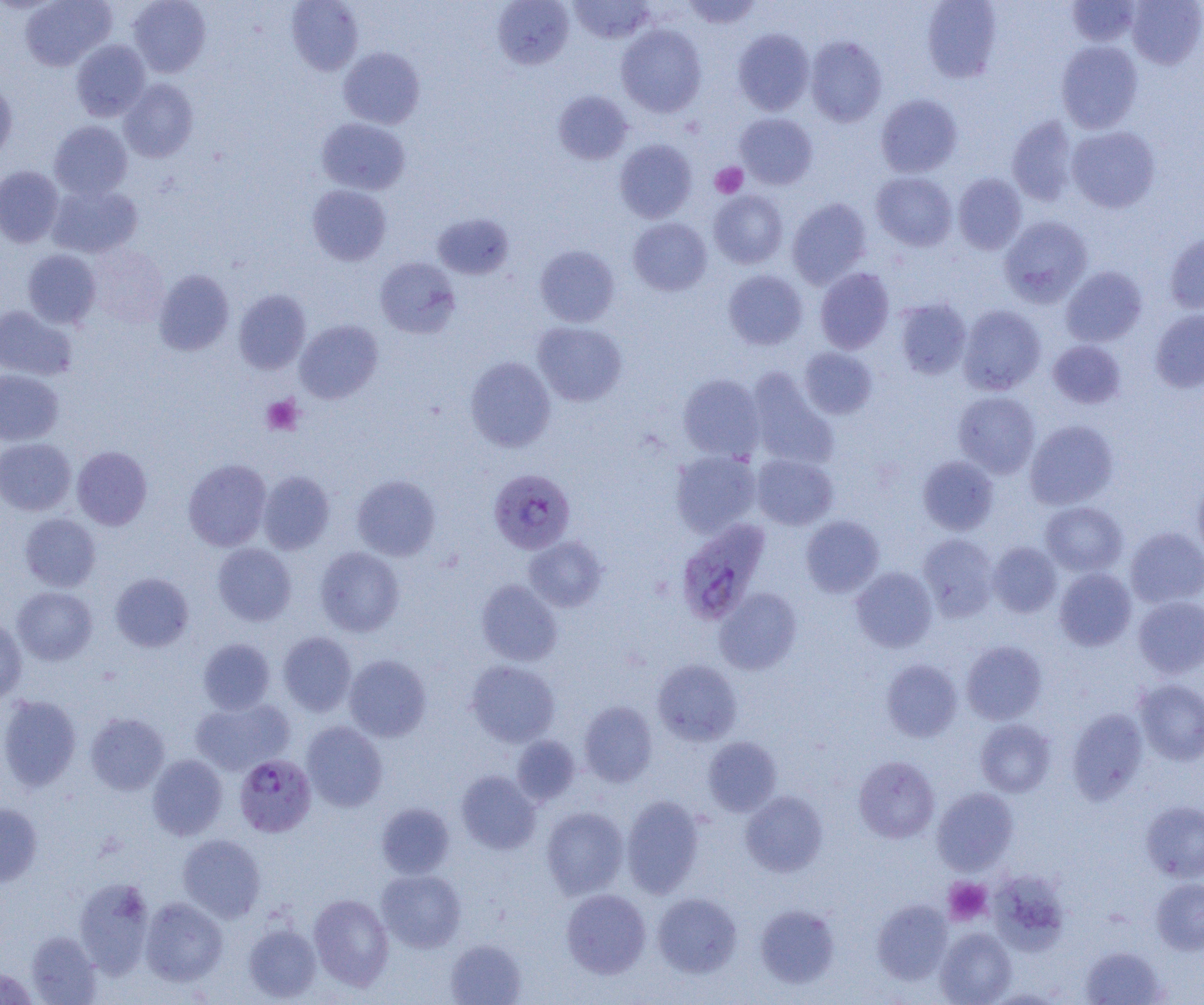
Summary:
  - Coordinate format: approximate bounding boxes as (x1,y1)-(x2,y2) corner pairs in pixels
  - Platelet locations: (711,162)-(748,198), (262,395)-(304,435), (944,877)-(993,926)
  - Uninfected red blood cell locations: (20,0)-(116,70), (128,0)-(211,77), (286,0)-(364,76), (680,0)-(763,29), (922,0)-(1002,83), (1126,0)-(1204,69), (492,1)-(575,69), (568,1)-(656,45), (1066,1)-(1141,47), (616,24)-(707,117), (732,28)-(815,115), (805,36)-(887,127), (71,39)-(150,121), (1056,40)-(1143,133), (338,47)-(425,129), (119,78)-(199,162), (0,82)-(17,162), (553,91)-(633,164), (876,94)-(962,177), (735,112)-(818,189), (1006,116)-(1079,206), (316,118)-(411,195), (49,120)-(132,200), (1067,125)-(1161,213), (615,140)-(697,222), (0,165)-(64,247), (871,171)-(957,251), (953,173)-(1027,254), (47,184)-(143,258), (307,185)-(392,266), (709,190)-(788,269), (787,198)-(872,288), (432,213)-(515,279), (999,216)-(1093,307), (628,217)-(712,296), (1164,232)-(1204,316), (87,244)-(168,327), (534,245)-(620,327), (23,249)-(101,328), (375,258)-(459,337), (1061,266)-(1147,347), (815,267)-(894,354), (153,269)-(235,356), (723,270)-(807,350), (233,289)-(311,374), (894,298)-(971,379), (0,305)-(77,380), (958,305)-(1046,395), (1149,309)-(1204,392), (295,320)-(383,404), (533,321)-(627,406), (1047,340)-(1126,409), (798,347)-(877,419), (465,356)-(555,452), (0,369)-(63,445), (746,369)-(839,471), (678,374)-(765,461), (953,391)-(1040,478), (1025,420)-(1119,509), (0,438)-(76,515), (72,445)-(152,530), (670,451)-(761,537), (751,454)-(839,530), (918,456)-(999,535), (183,458)-(272,551), (257,471)-(335,554), (351,475)-(441,561), (1192,477)-(1204,564), (1041,501)-(1128,576), (19,513)-(101,592), (800,515)-(884,597), (1125,527)-(1204,608), (918,533)-(999,621), (524,536)-(607,611), (987,542)-(1062,617), (212,543)-(296,626), (315,546)-(404,637), (851,566)-(938,652), (1054,568)-(1136,650), (110,572)-(194,652), (476,579)-(562,666), (12,586)-(98,665), (714,588)-(802,675), (1133,596)-(1204,679), (0,615)-(27,703), (278,632)-(357,716), (198,638)-(275,714), (961,640)-(1047,725), (344,654)-(431,742), (652,659)-(742,745), (881,659)-(962,741), (466,660)-(560,746), (1134,679)-(1204,765), (0,694)-(81,791), (191,698)-(293,775), (579,700)-(657,786), (1067,708)-(1149,803), (86,713)-(169,795), (975,719)-(1056,796), (301,721)-(388,811), (512,735)-(580,805), (703,737)-(782,816), (147,754)-(228,840), (854,756)-(939,843), (455,770)-(541,854), (932,787)-(1018,874), (740,790)-(828,877), (622,795)-(704,897), (1141,801)-(1204,882), (0,803)-(42,887), (376,803)-(455,878), (541,806)-(629,899), (178,834)-(266,922), (376,869)-(466,952), (993,872)-(1072,956), (74,877)-(155,976), (1151,877)-(1204,955), (561,888)-(651,978), (308,893)-(394,989), (652,893)-(742,977), (140,897)-(228,986), (872,900)-(952,985), (755,904)-(840,988), (243,923)-(321,1002), (935,927)-(1017,1005), (25,931)-(101,1005), (445,938)-(526,1005), (1080,946)-(1167,1005), (0,967)-(39,1004)
  - Plasmodium falciparum-infected red blood cell locations: (489,469)-(576,555), (677,517)-(772,628), (234,754)-(316,837)
  - Slide-level diagnosis: Plasmodium falciparum
  - Preparation: thin blood smear
  - Modality: optical microscopy
  - Field of view: one of a larger specimen
  - Image size: 1204×1005 pixels
  - Magnification: 1000x